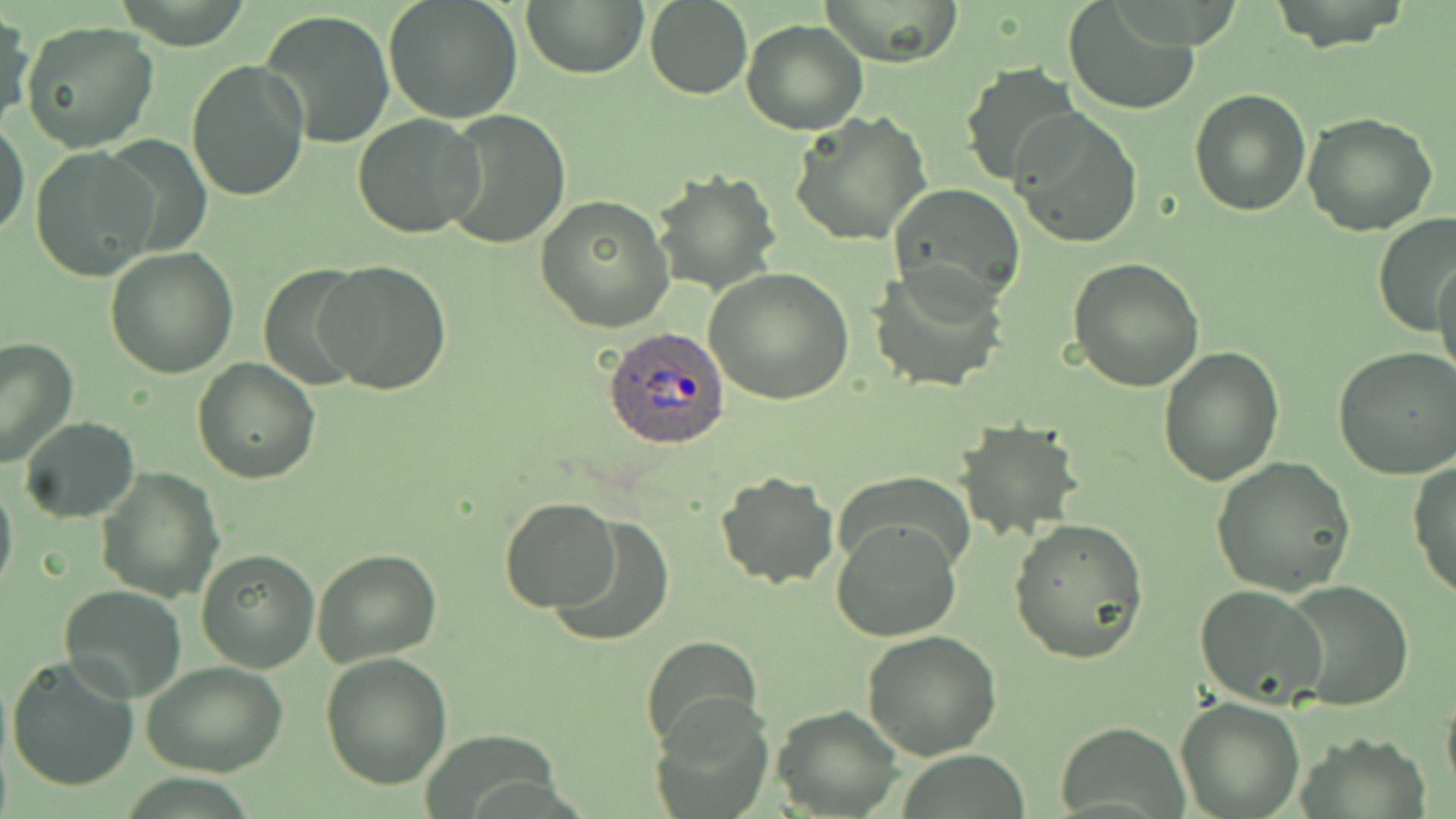

Approximate bounding boxes as named x1/y1/x2/y2 corners in pixels. Plasmodium ovale-infected red blood cell locations: (x1=602, y1=327, x2=731, y2=449). Uninfected red blood cell locations: (x1=384, y1=0, x2=523, y2=124), (x1=522, y1=0, x2=649, y2=78), (x1=817, y1=0, x2=964, y2=67), (x1=644, y1=1, x2=752, y2=99), (x1=1064, y1=2, x2=1201, y2=115), (x1=1263, y1=2, x2=1410, y2=52), (x1=259, y1=9, x2=395, y2=148), (x1=1, y1=11, x2=35, y2=132), (x1=741, y1=20, x2=869, y2=135), (x1=21, y1=21, x2=159, y2=154), (x1=186, y1=60, x2=310, y2=203), (x1=958, y1=65, x2=1083, y2=188), (x1=1188, y1=88, x2=1311, y2=216), (x1=437, y1=109, x2=572, y2=250), (x1=789, y1=109, x2=932, y2=247), (x1=1013, y1=110, x2=1143, y2=248), (x1=1301, y1=112, x2=1440, y2=236), (x1=353, y1=113, x2=484, y2=240), (x1=0, y1=118, x2=28, y2=240), (x1=30, y1=145, x2=159, y2=279), (x1=653, y1=170, x2=779, y2=297), (x1=888, y1=182, x2=1028, y2=308), (x1=534, y1=195, x2=675, y2=332), (x1=1372, y1=212, x2=1452, y2=336), (x1=104, y1=247, x2=238, y2=378), (x1=1435, y1=252, x2=1456, y2=388), (x1=1066, y1=258, x2=1205, y2=391), (x1=317, y1=260, x2=452, y2=395), (x1=256, y1=264, x2=368, y2=389), (x1=867, y1=264, x2=1009, y2=395), (x1=705, y1=268, x2=854, y2=405), (x1=0, y1=337, x2=78, y2=469), (x1=1158, y1=346, x2=1286, y2=485), (x1=1333, y1=346, x2=1456, y2=480), (x1=192, y1=358, x2=321, y2=482), (x1=19, y1=417, x2=139, y2=522), (x1=953, y1=418, x2=1080, y2=540), (x1=1212, y1=456, x2=1356, y2=596), (x1=1409, y1=460, x2=1456, y2=600), (x1=96, y1=466, x2=224, y2=602), (x1=714, y1=470, x2=838, y2=590), (x1=830, y1=470, x2=976, y2=577), (x1=0, y1=474, x2=18, y2=601), (x1=499, y1=497, x2=621, y2=612), (x1=548, y1=517, x2=675, y2=650), (x1=831, y1=518, x2=962, y2=642), (x1=1008, y1=518, x2=1150, y2=665), (x1=312, y1=546, x2=442, y2=667), (x1=196, y1=549, x2=321, y2=672), (x1=1279, y1=580, x2=1416, y2=712), (x1=60, y1=583, x2=187, y2=702), (x1=1193, y1=584, x2=1328, y2=710), (x1=862, y1=630, x2=1004, y2=757), (x1=641, y1=634, x2=763, y2=752), (x1=320, y1=652, x2=452, y2=791), (x1=6, y1=655, x2=140, y2=792), (x1=142, y1=660, x2=290, y2=778), (x1=1441, y1=680, x2=1456, y2=802), (x1=652, y1=695, x2=774, y2=818), (x1=1175, y1=698, x2=1304, y2=818), (x1=773, y1=705, x2=904, y2=817), (x1=1056, y1=724, x2=1188, y2=815). Slide-level diagnosis: Plasmodium ovale. Image is 1456×819 pixels. Light microscopy. May-Grünwald-Giemsa stain. Thin blood film. 1000x magnification. One field of a larger specimen.